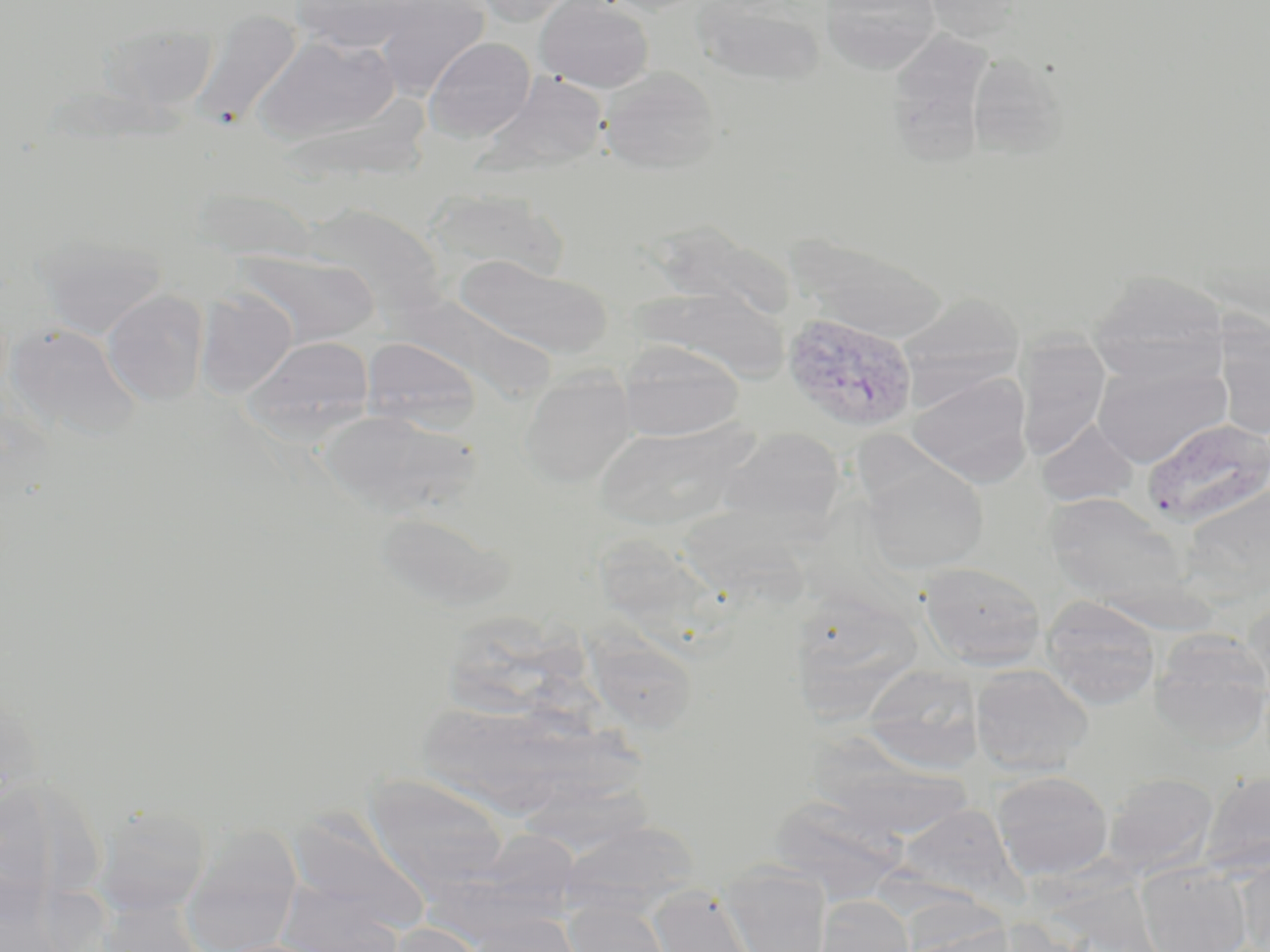
Approximate bounding boxes as (x1,y1)-(x2,y2) corner pairs in pixels. Plasmodium vivax-infected red blood cell locations: (781,311)-(917,432). Uninfected red blood cell locations: (290,0)-(417,52), (375,0)-(491,98), (472,0)-(583,27), (535,0)-(654,92), (923,0)-(1027,43), (692,1)-(828,86), (820,1)-(941,73), (192,8)-(302,130), (102,21)-(218,114), (886,29)-(995,166), (254,34)-(401,146), (424,37)-(535,142), (966,53)-(1068,158), (600,66)-(722,174), (485,72)-(611,174), (190,185)-(318,263), (426,188)-(566,285), (302,203)-(446,320), (648,220)-(797,321), (36,232)-(168,338), (793,237)-(949,342), (238,250)-(380,347), (455,255)-(612,359), (1088,270)-(1230,384), (636,285)-(790,383), (195,288)-(297,399), (102,289)-(210,406), (898,292)-(1025,399), (6,322)-(140,440), (1215,325)-(1270,438), (243,336)-(375,442), (1014,336)-(1111,461), (362,337)-(482,434), (616,341)-(745,442), (1092,357)-(1230,469), (518,369)-(637,487), (908,370)-(1033,487), (318,409)-(478,520), (1143,418)-(1270,527), (1037,420)-(1138,506), (593,421)-(752,531), (718,426)-(847,536), (861,457)-(989,574), (1180,481)-(1270,604), (1044,494)-(1190,609), (676,508)-(815,616), (373,510)-(514,613), (601,542)-(749,668), (918,561)-(1047,670), (787,592)-(923,724), (1041,596)-(1162,709), (1242,597)-(1270,701), (586,614)-(704,740), (1151,631)-(1270,749), (861,664)-(984,773), (970,664)-(1094,777), (429,705)-(647,814), (813,729)-(978,838), (991,770)-(1113,881), (1199,770)-(1270,877), (1102,771)-(1218,877), (363,773)-(507,897), (92,804)-(212,917), (779,805)-(908,898), (284,808)-(431,935), (558,819)-(701,919), (180,827)-(303,952), (1235,853)-(1270,952), (1136,863)-(1251,952), (721,864)-(832,952), (271,884)-(409,951), (647,885)-(763,952), (813,895)-(915,951), (91,898)-(210,952), (562,900)-(674,952), (462,914)-(584,952), (384,922)-(489,952). Slide-level diagnosis: Plasmodium vivax. Image is 1270×952 pixels. May-Grünwald-Giemsa stain. Optical microscopy. Captured at 1000x magnification. Thin blood smear. Single field of view.